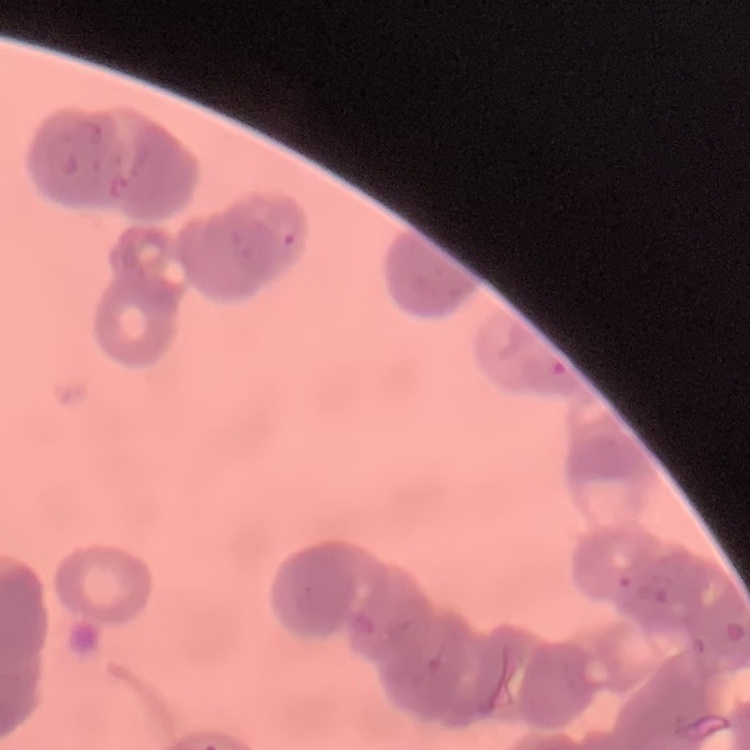

Summary:
  - Red blood cell morphology: rouleaux formation
  - Image type: square crop of a larger photomicrograph
  - Stain: Field's or Giemsa
  - Preparation: thin blood smear